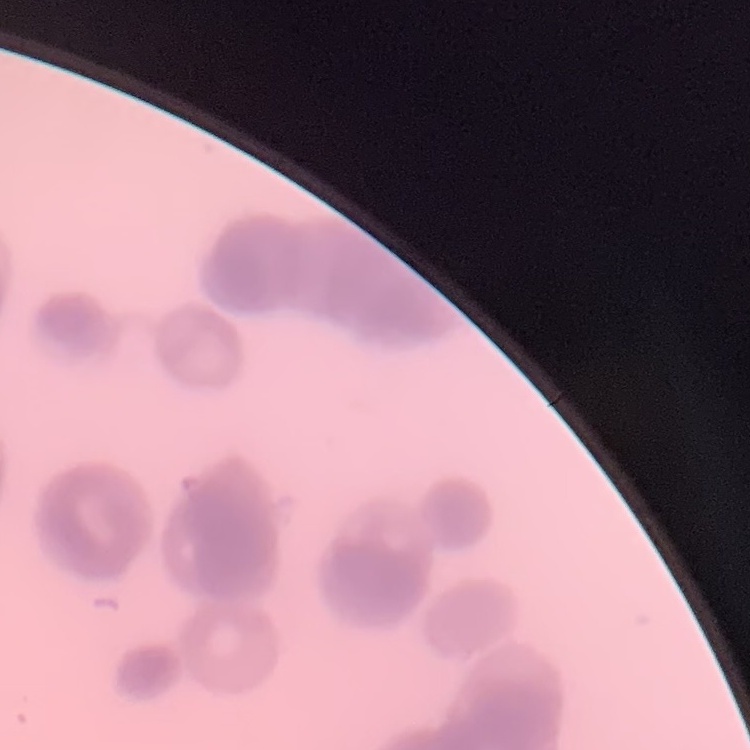

Summary:
  - Erythrocyte morphology: rouleaux formation
  - Image type: one tile cut from a larger photomicrograph
  - Preparation: thin peripheral smear
  - Stain: Field's or Giemsa